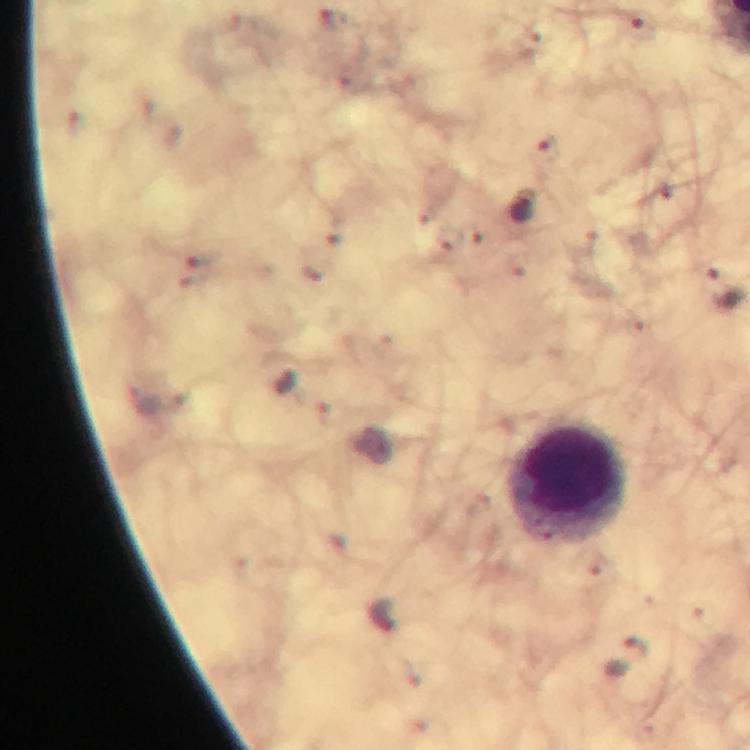

{
  "image_size": "750×750 pixels",
  "leukocyte_locations": "approximate centers as (x, y) in pixels: (566, 481)",
  "capture": "smartphone mounted on the microscope",
  "immersion_oil": "applied",
  "magnification": "100x",
  "context": "from a diagnostic examination for malaria",
  "stain": "Giemsa",
  "cropped_from": "one field of view",
  "preparation": "thick smear",
  "plasmodium_parasite_locations": "approximate centers as (x, y) in pixels: (639, 27), (521, 206), (627, 659)"
}